Comment on the morphology of the erythrocytes.
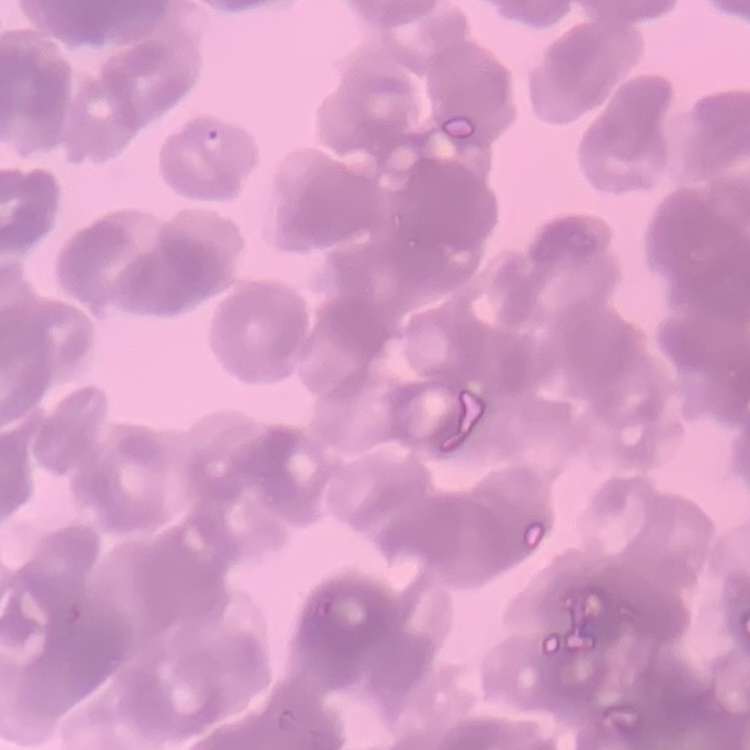

Rouleaux formation.

Field's or Giemsa stain. Thin blood film. One tile cut from a larger photomicrograph.